Identify the parasite.
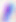
Toxoplasma gondii.

Summary:
  - Magnification: 400x
  - Modality: photomicrograph